Outline each Plasmodium falciparum-infected red blood cell.
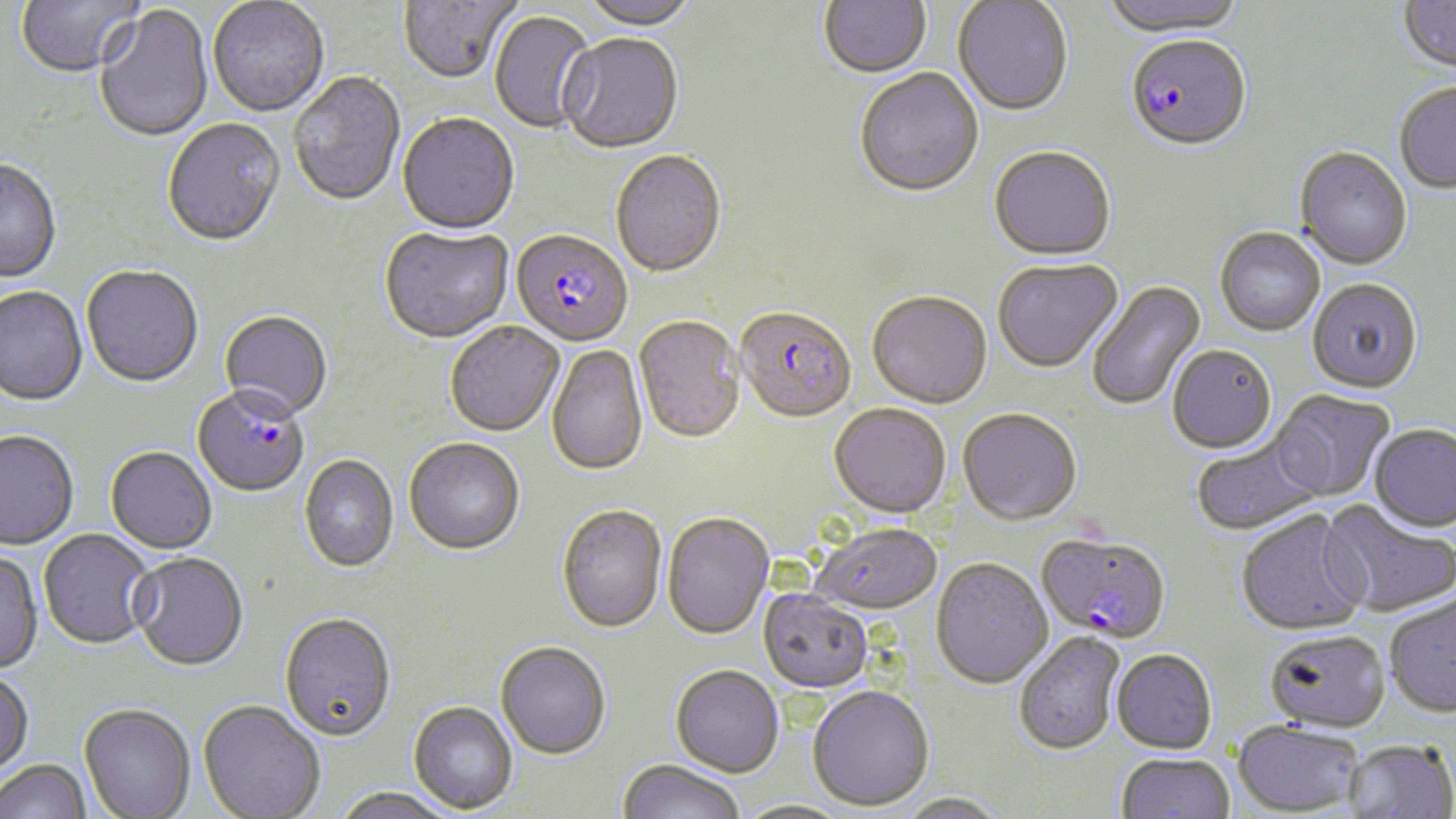
Approximate bounding boxes as named x1/y1/x2/y2 corners in pixels.
Plasmodium falciparum-infected red blood cells: (x1=1125, y1=38, x2=1252, y2=154), (x1=510, y1=232, x2=633, y2=349), (x1=735, y1=308, x2=856, y2=425), (x1=192, y1=389, x2=309, y2=499), (x1=1036, y1=532, x2=1171, y2=644).

Uninfected red blood cell locations: (x1=15, y1=0, x2=145, y2=80), (x1=208, y1=0, x2=330, y2=119), (x1=398, y1=0, x2=519, y2=86), (x1=581, y1=0, x2=698, y2=32), (x1=819, y1=0, x2=931, y2=80), (x1=1101, y1=0, x2=1247, y2=40), (x1=953, y1=1, x2=1073, y2=119), (x1=1398, y1=1, x2=1456, y2=76), (x1=94, y1=5, x2=214, y2=144), (x1=489, y1=11, x2=597, y2=135), (x1=558, y1=36, x2=683, y2=156), (x1=854, y1=70, x2=984, y2=200), (x1=289, y1=73, x2=406, y2=209), (x1=1393, y1=84, x2=1456, y2=194), (x1=398, y1=115, x2=520, y2=237), (x1=163, y1=120, x2=286, y2=249), (x1=989, y1=148, x2=1116, y2=263), (x1=1295, y1=148, x2=1413, y2=271), (x1=611, y1=152, x2=726, y2=280), (x1=0, y1=160, x2=62, y2=285), (x1=1215, y1=227, x2=1326, y2=336), (x1=379, y1=228, x2=514, y2=345), (x1=992, y1=259, x2=1123, y2=374), (x1=81, y1=267, x2=203, y2=389), (x1=1307, y1=278, x2=1423, y2=394), (x1=1086, y1=279, x2=1206, y2=412), (x1=0, y1=287, x2=88, y2=408), (x1=867, y1=293, x2=992, y2=410), (x1=219, y1=312, x2=333, y2=424), (x1=634, y1=317, x2=745, y2=446), (x1=445, y1=323, x2=564, y2=439), (x1=1168, y1=344, x2=1277, y2=453), (x1=547, y1=345, x2=648, y2=477), (x1=1270, y1=388, x2=1396, y2=502), (x1=829, y1=403, x2=951, y2=518), (x1=958, y1=408, x2=1081, y2=525), (x1=1369, y1=424, x2=1456, y2=532), (x1=0, y1=433, x2=79, y2=551), (x1=1190, y1=435, x2=1323, y2=536), (x1=404, y1=440, x2=525, y2=557), (x1=105, y1=448, x2=217, y2=555), (x1=299, y1=456, x2=399, y2=574), (x1=1320, y1=501, x2=1456, y2=618), (x1=557, y1=506, x2=667, y2=635), (x1=1236, y1=509, x2=1371, y2=637), (x1=663, y1=512, x2=774, y2=639), (x1=810, y1=522, x2=943, y2=615), (x1=38, y1=530, x2=157, y2=651), (x1=0, y1=551, x2=44, y2=675), (x1=130, y1=554, x2=249, y2=673), (x1=932, y1=558, x2=1053, y2=689), (x1=759, y1=590, x2=873, y2=693), (x1=1384, y1=592, x2=1456, y2=717), (x1=279, y1=614, x2=396, y2=744), (x1=1264, y1=628, x2=1390, y2=732), (x1=1013, y1=632, x2=1125, y2=756), (x1=496, y1=643, x2=610, y2=761), (x1=1111, y1=650, x2=1217, y2=754), (x1=670, y1=665, x2=785, y2=778), (x1=0, y1=670, x2=35, y2=779), (x1=807, y1=685, x2=934, y2=811), (x1=197, y1=701, x2=325, y2=819), (x1=409, y1=702, x2=518, y2=815), (x1=79, y1=706, x2=195, y2=819), (x1=1232, y1=720, x2=1365, y2=816), (x1=1344, y1=738, x2=1456, y2=818), (x1=1115, y1=752, x2=1235, y2=819), (x1=617, y1=759, x2=746, y2=819), (x1=0, y1=761, x2=91, y2=819), (x1=331, y1=788, x2=455, y2=819), (x1=897, y1=791, x2=1008, y2=819), (x1=732, y1=799, x2=855, y2=818). Slide-level diagnosis: Plasmodium falciparum. May-Grünwald-Giemsa stain. Optical microscopy. Thin blood film. Image is 1456×819 pixels. Captured at 1000x magnification. One field of a larger specimen.